Identify the cell.
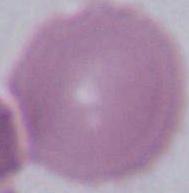
This is an erythrocyte.

Captured at 1000x magnification. Photomicrograph.